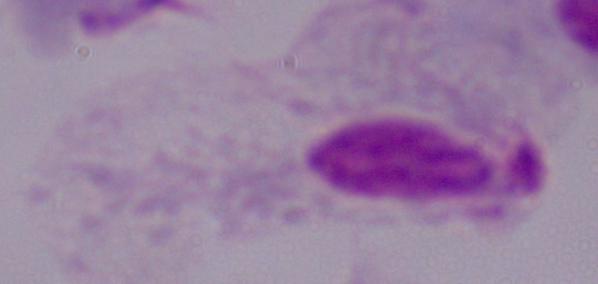

Captured at 1000x magnification. Micrograph. A trichomonad is seen.